Report the malaria status of this cell.
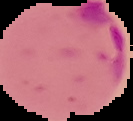

It is parasitized.

Summary:
  - Preparation: thin blood smear
  - Image type: cell region segmented out of the field of view; surrounding area masked to black
  - Image size: 133×121 pixels